Identify the cell.
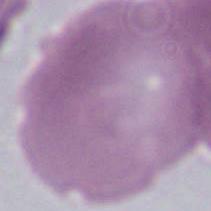

An erythrocyte.

Summary:
  - Magnification: 1000x
  - Modality: photomicrograph